Describe the morphology of the red blood cells.
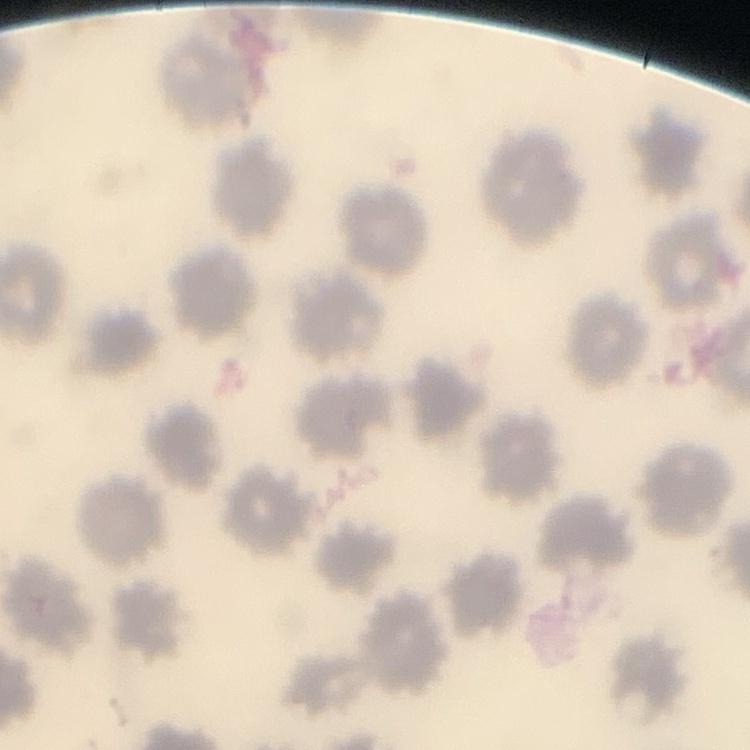

They show no rouleaux formation.

Thin blood smear. One tile cut from a larger photomicrograph. Field's or Giemsa stain.